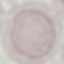

Summary:
  - Malaria status: uninfected
  - Capture: smartphone through the microscope eyepiece
  - Stain: Giemsa
  - Preparation: thin smear
  - Image type: automatically extracted cell patch, resized to 64 × 64 pixels